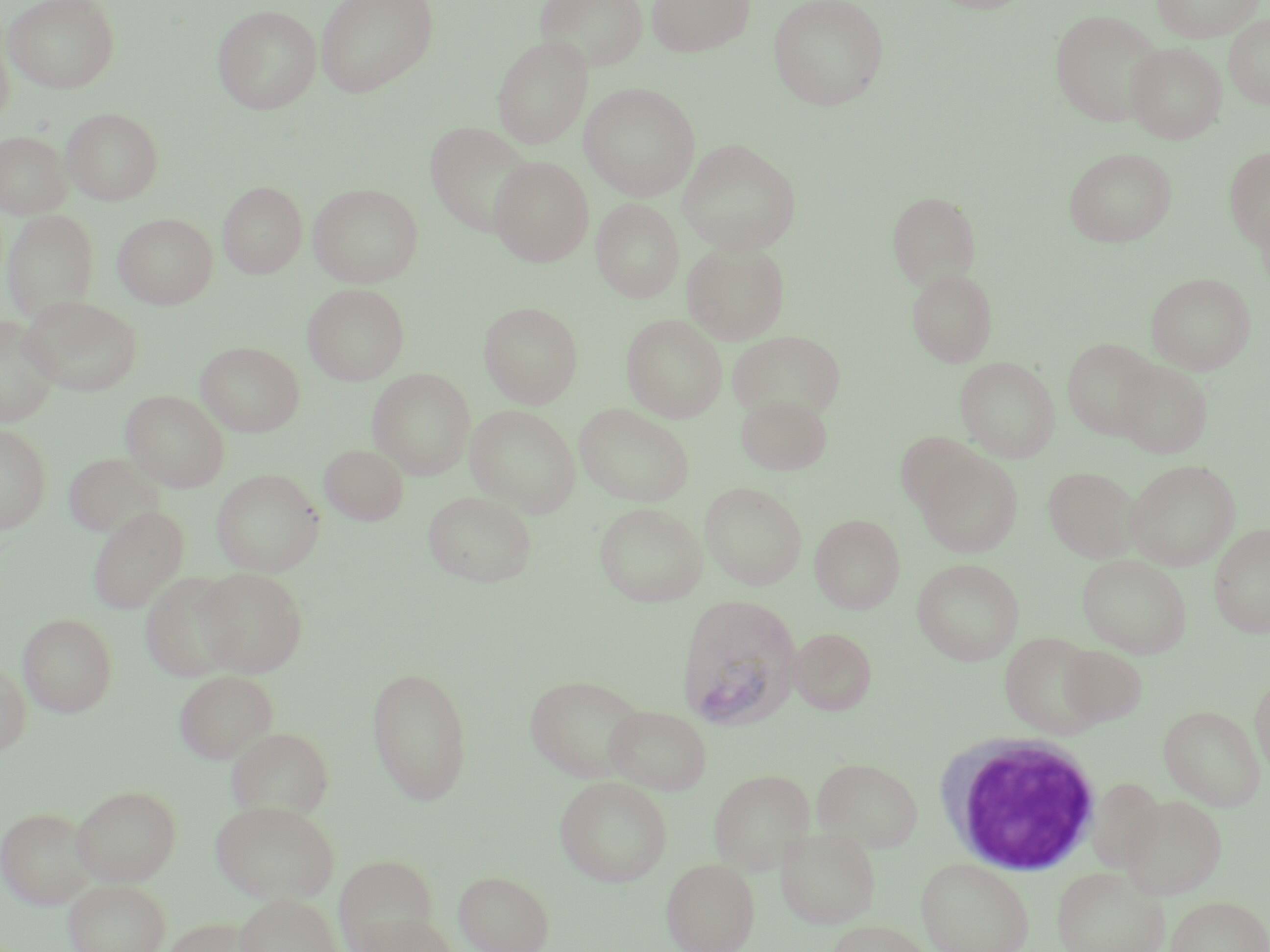

slide-level diagnosis = Plasmodium vivax
white blood cell locations = approximate bounding boxes as named x1/y1/x2/y2 corners in pixels: (x1=934, y1=732, x2=1103, y2=875)
stain = May-Grünwald-Giemsa
magnification = 1000x
uninfected red blood cell locations = approximate bounding boxes as named x1/y1/x2/y2 corners in pixels: (x1=3, y1=0, x2=120, y2=92), (x1=315, y1=0, x2=438, y2=98), (x1=534, y1=0, x2=647, y2=71), (x1=646, y1=0, x2=754, y2=57), (x1=768, y1=0, x2=890, y2=110), (x1=1151, y1=0, x2=1264, y2=42), (x1=212, y1=4, x2=322, y2=114), (x1=1049, y1=8, x2=1164, y2=126), (x1=1224, y1=14, x2=1270, y2=108), (x1=0, y1=25, x2=14, y2=128), (x1=493, y1=35, x2=592, y2=148), (x1=1125, y1=41, x2=1227, y2=143), (x1=579, y1=81, x2=700, y2=200), (x1=61, y1=107, x2=164, y2=205), (x1=425, y1=121, x2=535, y2=237), (x1=0, y1=130, x2=73, y2=219), (x1=678, y1=139, x2=801, y2=255), (x1=1224, y1=146, x2=1270, y2=250), (x1=1064, y1=147, x2=1177, y2=247), (x1=490, y1=156, x2=594, y2=266), (x1=218, y1=181, x2=307, y2=278), (x1=308, y1=183, x2=423, y2=287), (x1=887, y1=191, x2=981, y2=290), (x1=591, y1=198, x2=684, y2=302), (x1=1254, y1=198, x2=1270, y2=298), (x1=2, y1=209, x2=99, y2=323), (x1=113, y1=213, x2=218, y2=309), (x1=682, y1=241, x2=790, y2=344), (x1=906, y1=267, x2=998, y2=367), (x1=1146, y1=272, x2=1256, y2=375), (x1=303, y1=283, x2=410, y2=385), (x1=21, y1=295, x2=142, y2=396), (x1=479, y1=301, x2=583, y2=407), (x1=621, y1=314, x2=728, y2=422), (x1=0, y1=316, x2=60, y2=427), (x1=729, y1=330, x2=845, y2=421), (x1=1062, y1=338, x2=1160, y2=440), (x1=196, y1=341, x2=304, y2=436), (x1=955, y1=356, x2=1060, y2=462), (x1=1116, y1=361, x2=1212, y2=458), (x1=368, y1=368, x2=476, y2=480), (x1=121, y1=390, x2=229, y2=492), (x1=736, y1=392, x2=832, y2=474), (x1=574, y1=403, x2=695, y2=506), (x1=466, y1=405, x2=580, y2=517), (x1=0, y1=424, x2=51, y2=533), (x1=896, y1=432, x2=985, y2=516), (x1=319, y1=444, x2=409, y2=524), (x1=64, y1=452, x2=165, y2=537), (x1=917, y1=452, x2=1023, y2=557), (x1=1126, y1=459, x2=1240, y2=570), (x1=1044, y1=466, x2=1140, y2=563), (x1=212, y1=468, x2=324, y2=576), (x1=700, y1=481, x2=807, y2=590), (x1=423, y1=490, x2=537, y2=587), (x1=594, y1=502, x2=708, y2=606), (x1=88, y1=505, x2=189, y2=614), (x1=810, y1=514, x2=905, y2=613), (x1=1209, y1=522, x2=1270, y2=639), (x1=1077, y1=554, x2=1191, y2=657), (x1=912, y1=558, x2=1024, y2=665), (x1=195, y1=567, x2=309, y2=676), (x1=140, y1=571, x2=244, y2=680), (x1=17, y1=612, x2=118, y2=717), (x1=789, y1=628, x2=877, y2=715), (x1=1000, y1=632, x2=1104, y2=737), (x1=1058, y1=645, x2=1148, y2=726), (x1=0, y1=661, x2=31, y2=757), (x1=366, y1=665, x2=473, y2=805), (x1=175, y1=670, x2=277, y2=764), (x1=1250, y1=671, x2=1270, y2=782), (x1=525, y1=673, x2=649, y2=782), (x1=604, y1=704, x2=712, y2=795), (x1=1159, y1=704, x2=1266, y2=811), (x1=224, y1=726, x2=335, y2=817), (x1=811, y1=756, x2=924, y2=852), (x1=708, y1=768, x2=816, y2=874), (x1=555, y1=775, x2=673, y2=887), (x1=1086, y1=777, x2=1166, y2=871), (x1=71, y1=785, x2=181, y2=885), (x1=1120, y1=793, x2=1227, y2=899), (x1=212, y1=800, x2=338, y2=903), (x1=0, y1=806, x2=96, y2=908), (x1=776, y1=826, x2=880, y2=928), (x1=334, y1=854, x2=437, y2=950), (x1=662, y1=858, x2=760, y2=952), (x1=917, y1=858, x2=1033, y2=952), (x1=1051, y1=865, x2=1169, y2=952), (x1=454, y1=870, x2=554, y2=952), (x1=63, y1=879, x2=171, y2=952), (x1=235, y1=893, x2=342, y2=952), (x1=1166, y1=895, x2=1270, y2=952), (x1=357, y1=913, x2=458, y2=952), (x1=162, y1=917, x2=263, y2=952), (x1=826, y1=919, x2=935, y2=952)
image size = 1270×952 pixels
preparation = thin blood film
field of view = single
Plasmodium vivax-infected red blood cell locations = approximate bounding boxes as named x1/y1/x2/y2 corners in pixels: (x1=675, y1=593, x2=802, y2=730)
modality = optical microscopy